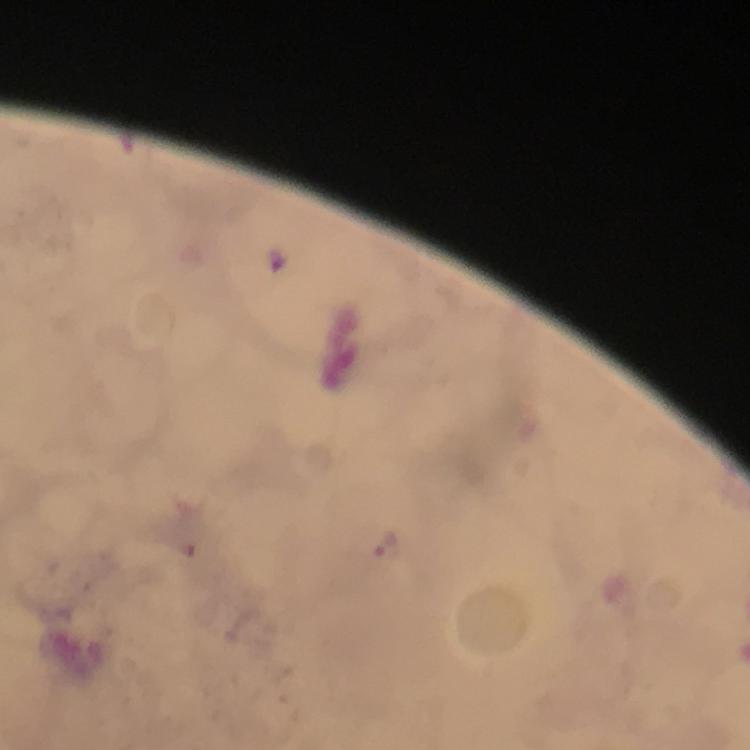

stain: Giemsa
cropped_from: a single field of view
magnification: 100x
capture: smartphone camera through the microscope
malaria_parasite_locations: 'approximate centers as (x, y) in pixels: (385, 543)'
immersion_oil: used
preparation: thick blood smear
context: from a malaria diagnostic workup
image_size: 750×750 pixels